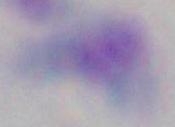

magnification: 1000x
modality: micrograph
identification: Toxoplasma gondii